State the blood parasite species.
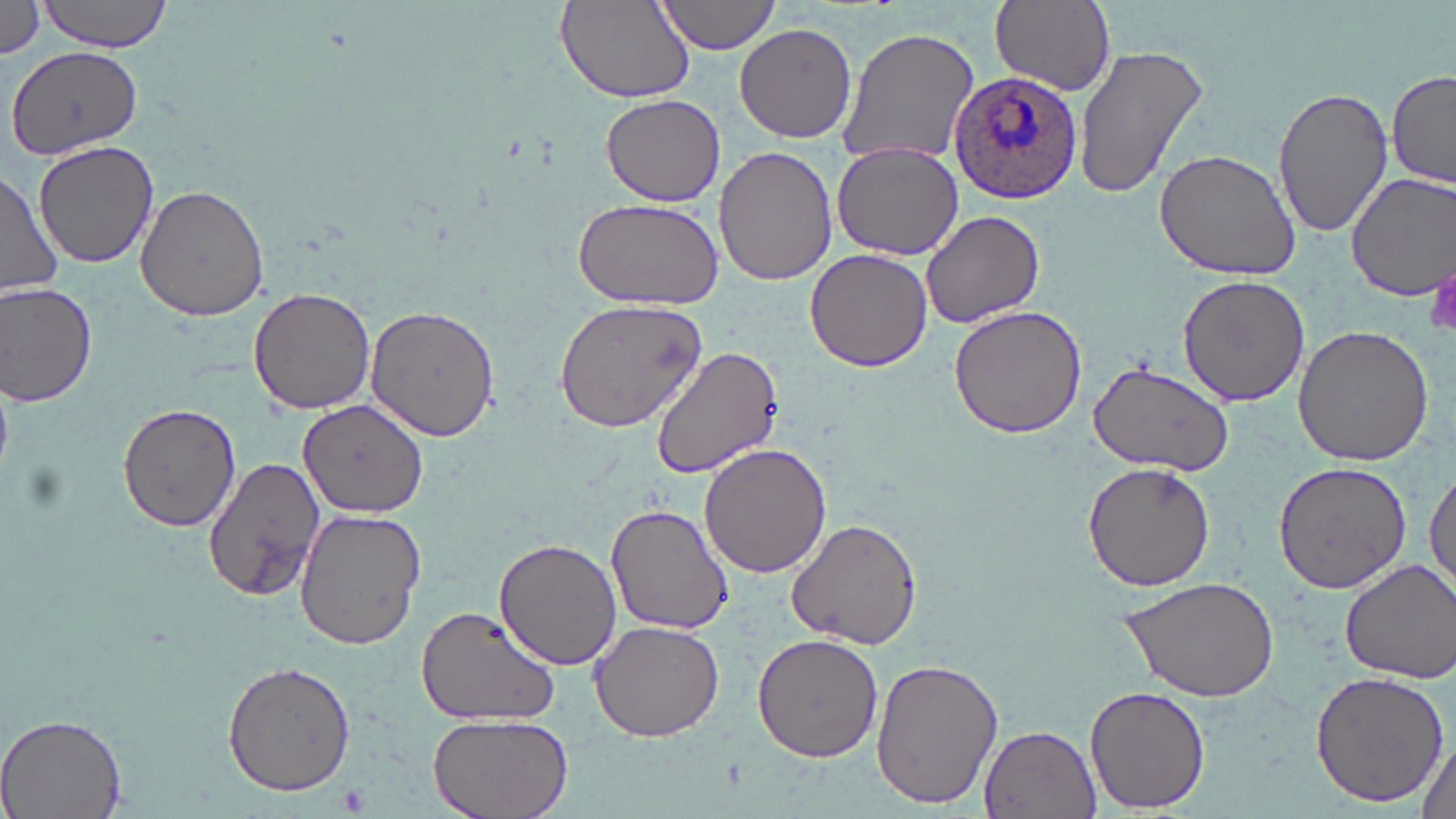

Plasmodium ovale.

uninfected_red_blood_cell_locations: 'approximate bounding boxes as [x1, y1, x2, y2] in pixels: [39, 0, 175, 53], [556, 0, 696, 103], [654, 0, 780, 56], [987, 0, 1115, 97], [0, 4, 48, 59], [735, 23, 857, 143], [836, 26, 979, 172], [1071, 43, 1209, 199], [6, 44, 144, 162], [1387, 70, 1456, 189], [1274, 85, 1394, 239], [601, 94, 727, 205], [32, 139, 161, 268], [831, 140, 964, 260], [712, 144, 837, 287], [1154, 149, 1304, 281], [0, 170, 61, 301], [1343, 171, 1456, 301], [137, 183, 272, 322], [573, 197, 725, 312], [919, 210, 1047, 330], [804, 248, 933, 373], [1176, 276, 1311, 408], [0, 282, 98, 407], [248, 286, 375, 414], [554, 299, 705, 432], [366, 304, 500, 441], [949, 305, 1087, 439], [1292, 325, 1434, 468], [652, 345, 783, 477], [1087, 359, 1236, 477], [298, 398, 428, 518], [118, 401, 241, 533], [698, 444, 832, 579], [203, 456, 326, 603], [1082, 461, 1216, 593], [1425, 461, 1456, 599], [1271, 462, 1412, 593], [605, 502, 735, 636], [294, 507, 425, 651], [787, 516, 924, 649], [493, 538, 625, 670], [1339, 559, 1456, 684], [1120, 576, 1281, 700], [414, 603, 561, 726], [589, 621, 724, 742], [752, 634, 883, 762], [870, 654, 1006, 810], [221, 659, 357, 796], [1309, 670, 1448, 808], [1085, 684, 1211, 815], [1, 711, 128, 819], [424, 713, 574, 819], [980, 725, 1102, 817], [1414, 734, 1456, 819]'
magnification: 1000x
image_size: 1456×819 pixels
preparation: thin blood film
platelet_locations: 'approximate bounding boxes as [x1, y1, x2, y2] in pixels: [1427, 265, 1456, 340]'
field_of_view: one of a larger specimen
plasmodium_ovale_infected_red_blood_cell_locations: 'approximate bounding boxes as [x1, y1, x2, y2] in pixels: [948, 71, 1083, 205]'
stain: May-Grünwald-Giemsa
modality: light microscopy